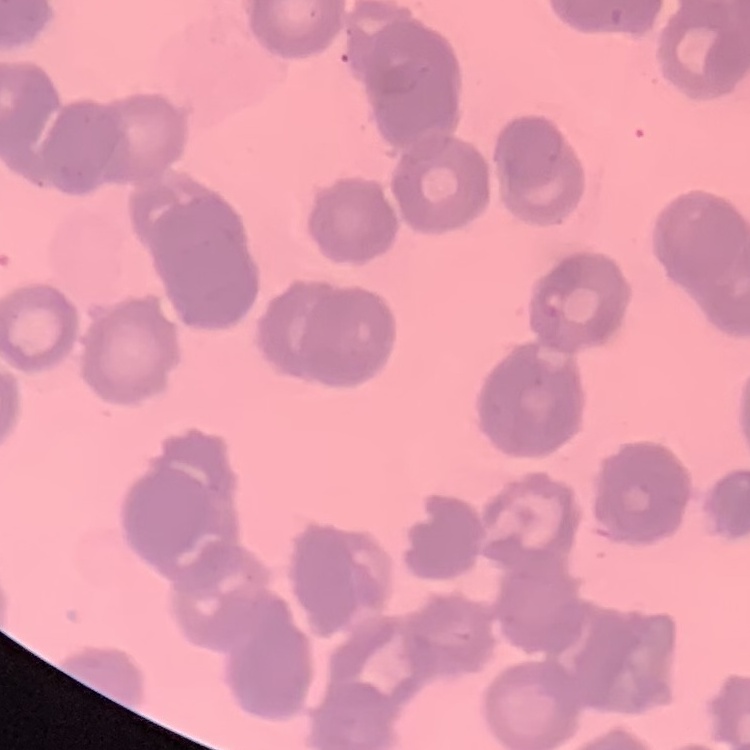 The erythrocytes show rouleaux formation. Field's or Giemsa stain. One tile cut from a larger photomicrograph. Thin peripheral smear.